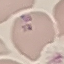

Summary:
  - Result: malaria parasites identified
  - Capture: smartphone camera at the microscope eyepiece
  - Image type: cell patch, automatically extracted from a larger field of view and resized to 64 × 64 pixels
  - Stain: Giemsa
  - Preparation: thin smear